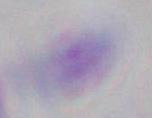

{
  "modality": "photomicrograph",
  "magnification": "1000x",
  "identification": "Toxoplasma gondii"
}